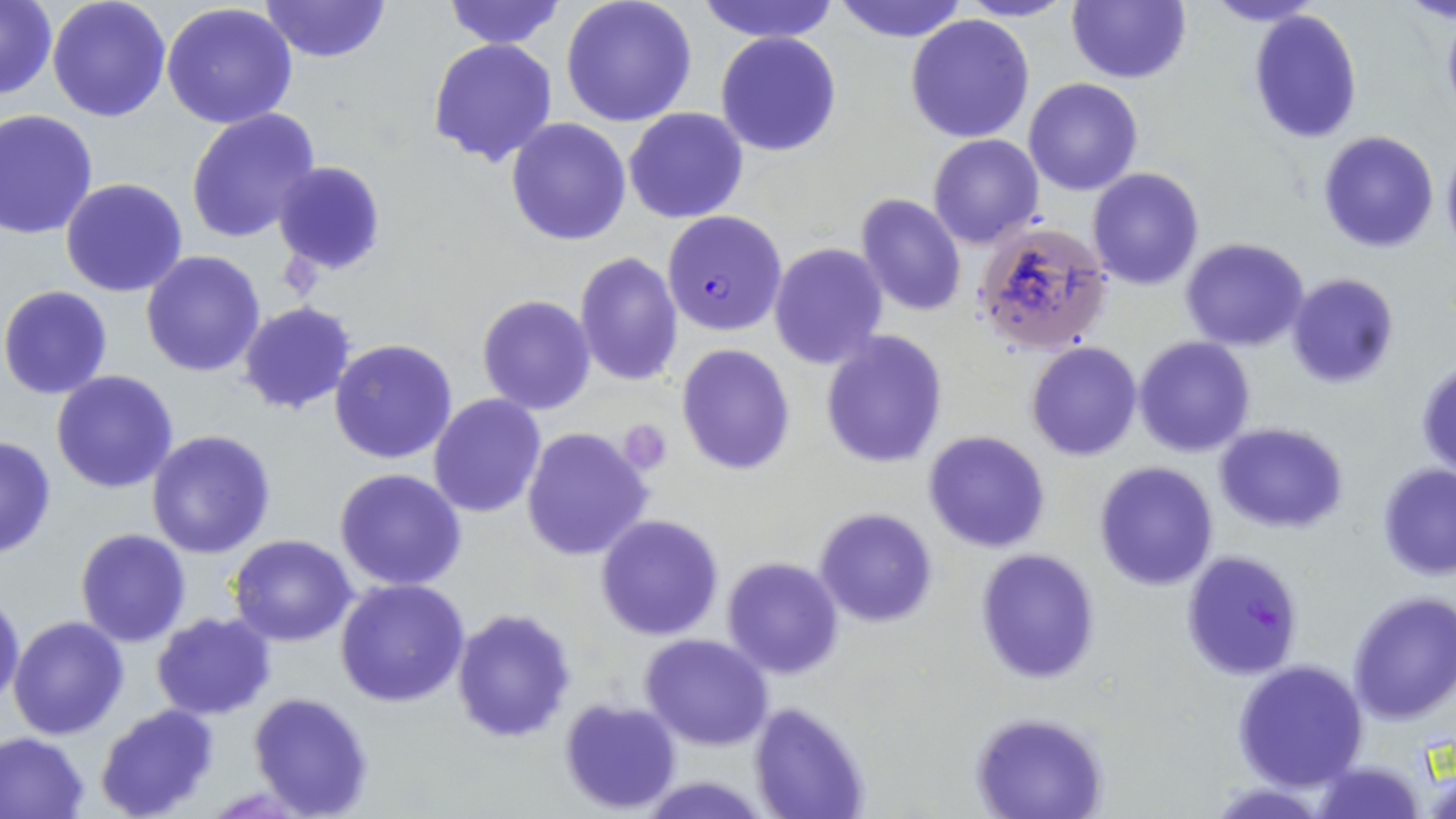

Summary:
  - Coordinate format: approximate bounding boxes as (x1, y1, x2, y2) in pixels
  - Uninfected red blood cell locations: (47, 0, 172, 122), (261, 0, 389, 64), (442, 0, 565, 49), (559, 0, 698, 126), (697, 0, 840, 43), (953, 0, 1076, 22), (1067, 0, 1191, 84), (1204, 0, 1327, 28), (1, 1, 56, 102), (831, 1, 971, 42), (161, 5, 299, 131), (1246, 9, 1362, 144), (905, 13, 1034, 143), (715, 31, 841, 157), (427, 38, 559, 167), (1024, 77, 1144, 196), (0, 108, 100, 239), (624, 108, 749, 224), (186, 109, 320, 243), (506, 116, 633, 246), (1316, 130, 1440, 252), (928, 134, 1044, 248), (1440, 141, 1456, 255), (274, 161, 385, 275), (1087, 167, 1204, 289), (60, 178, 188, 297), (855, 192, 967, 317), (976, 223, 1112, 354), (1180, 237, 1310, 351), (769, 242, 888, 369), (141, 250, 267, 377), (574, 251, 682, 386), (1286, 273, 1399, 390), (1, 285, 115, 399), (478, 294, 596, 414), (238, 302, 358, 416), (819, 330, 949, 469), (1135, 337, 1256, 457), (329, 339, 459, 465), (1025, 341, 1142, 461), (677, 344, 797, 475), (1415, 358, 1456, 478), (50, 371, 179, 495), (428, 394, 546, 518), (1214, 423, 1349, 532), (522, 426, 653, 561), (146, 430, 276, 558), (922, 430, 1052, 554), (0, 433, 58, 560), (1094, 462, 1218, 590), (1376, 463, 1455, 580), (334, 468, 468, 592), (814, 507, 939, 628), (595, 515, 724, 641), (76, 528, 191, 647), (228, 533, 358, 645), (976, 548, 1101, 685), (722, 557, 846, 679), (335, 578, 469, 707), (1347, 591, 1456, 722), (0, 592, 24, 706), (452, 607, 576, 743), (151, 612, 275, 719), (7, 615, 127, 740), (641, 635, 773, 750), (1232, 659, 1368, 790), (247, 691, 375, 817), (558, 698, 682, 815), (748, 701, 871, 819), (95, 702, 222, 819), (971, 712, 1109, 819), (0, 731, 90, 819), (1419, 749, 1456, 819), (1313, 759, 1425, 819), (638, 775, 772, 816)
  - Plasmodium falciparum-infected red blood cell locations: (662, 210, 787, 335), (1180, 550, 1304, 680)
  - Platelet locations: (279, 253, 327, 298), (618, 419, 673, 477)
  - Slide-level diagnosis: Plasmodium falciparum
  - Field of view: one of a larger specimen
  - Magnification: 1000x
  - Modality: light microscopy
  - Stain: May-Grünwald-Giemsa
  - Image size: 1456×819 pixels
  - Preparation: thin blood smear